Assess this cell for malaria.
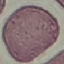

Uninfected.

Thin blood film. Giemsa stain. Photographed with a smartphone camera at the microscope eyepiece. Automatically extracted cell patch, resized to 64 × 64 pixels.